Assess the morphology of the erythrocytes.
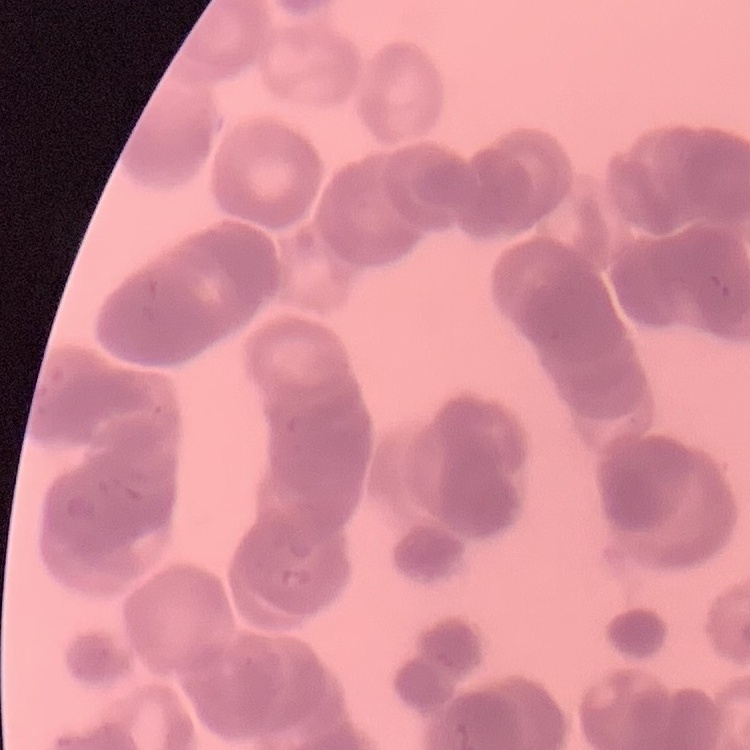

They show rouleaux formation.

Summary:
  - Image type: one tile cut from a larger photomicrograph
  - Stain: Field's or Giemsa
  - Preparation: thin peripheral smear